Outline each Plasmodium falciparum parasite and classify it by life-cycle stage.
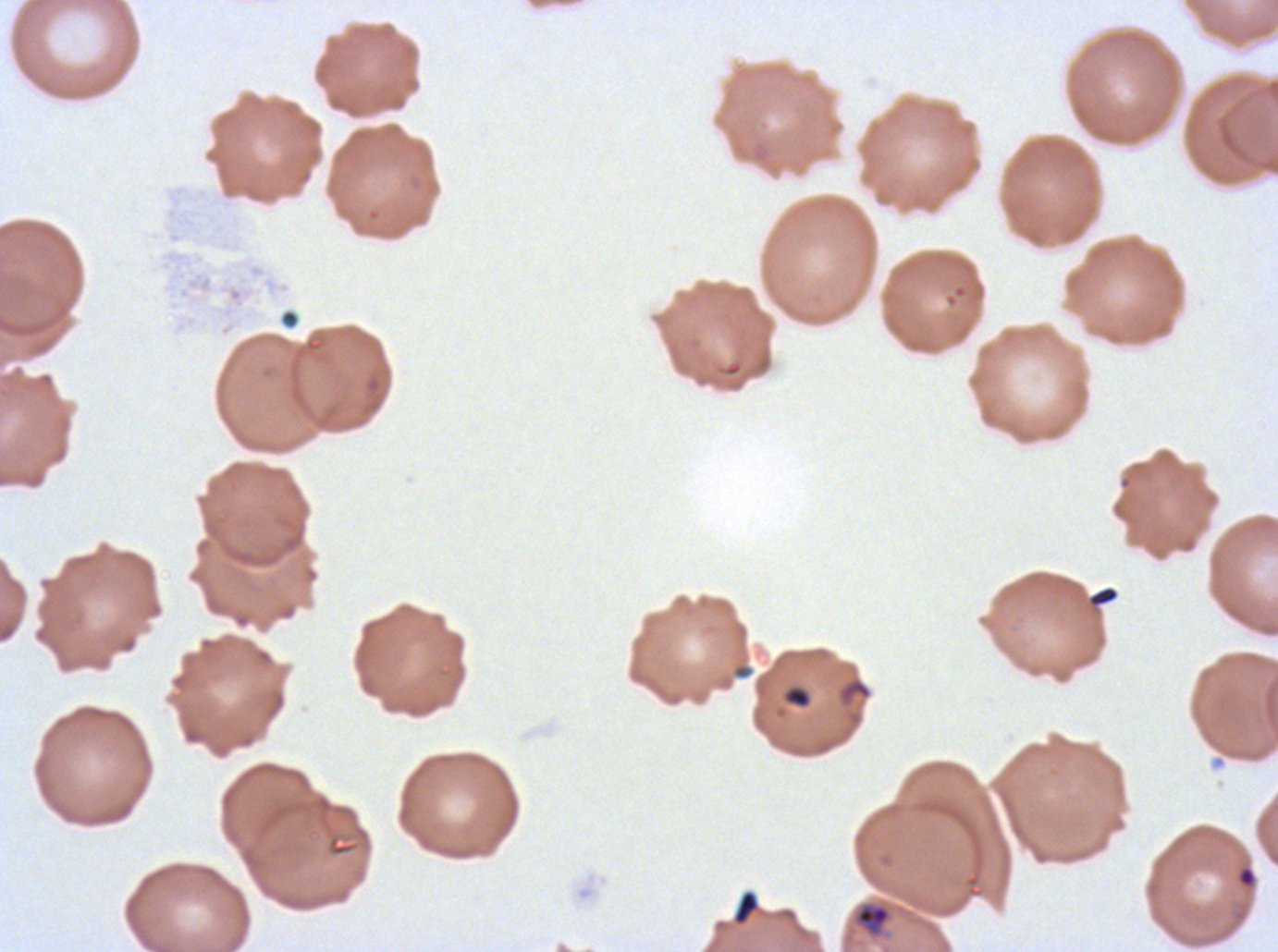

Approximate bounding boxes as (x1, y1, x2, y2) in pixels.
Rings: (1237, 866, 1257, 887).
Late trophozoites: (855, 904, 891, 934).
No late-ring/early-trophozoite forms, mid trophozoites, early schizonts, late schizonts, segmenters, or gametocytes observed.

Summary:
  - Debris locations: (1088, 585, 1119, 608), (731, 663, 754, 680), (782, 685, 812, 709), (733, 890, 758, 924)
  - Life-cycle stages observed: ring, late trophozoite
  - Stain: Giemsa
  - Specimen: ex-vivo Plasmodium falciparum culture from a patient in The Gambia, grown for 24 to 48 hours
  - Image size: 1278×952 pixels
  - Field of view: one sub-image of a larger composite
  - Preparation: thin blood film